Assess for malaria.
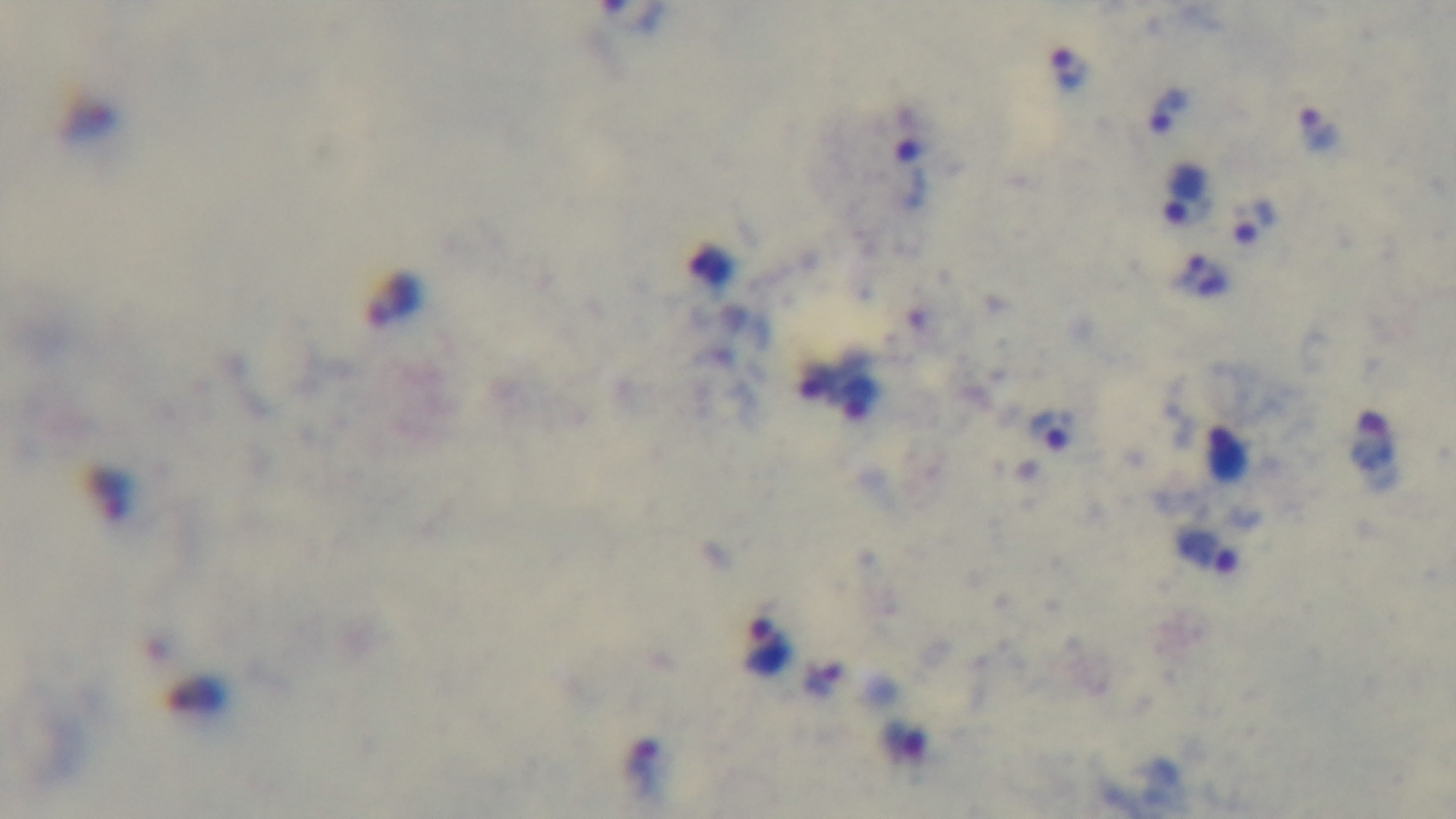

It is infected.

Summary:
  - Stain: Giemsa
  - Preparation: thick smear
  - Field of view: single
  - Capture: mounted 4K digital camera
  - Modality: light microscopy
  - Objective: 100x oil immersion